Report the malaria status of this cell.
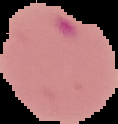
It is parasitized.

From a thin blood smear. Segmented cell region on a black background. Image is 118×124 pixels.